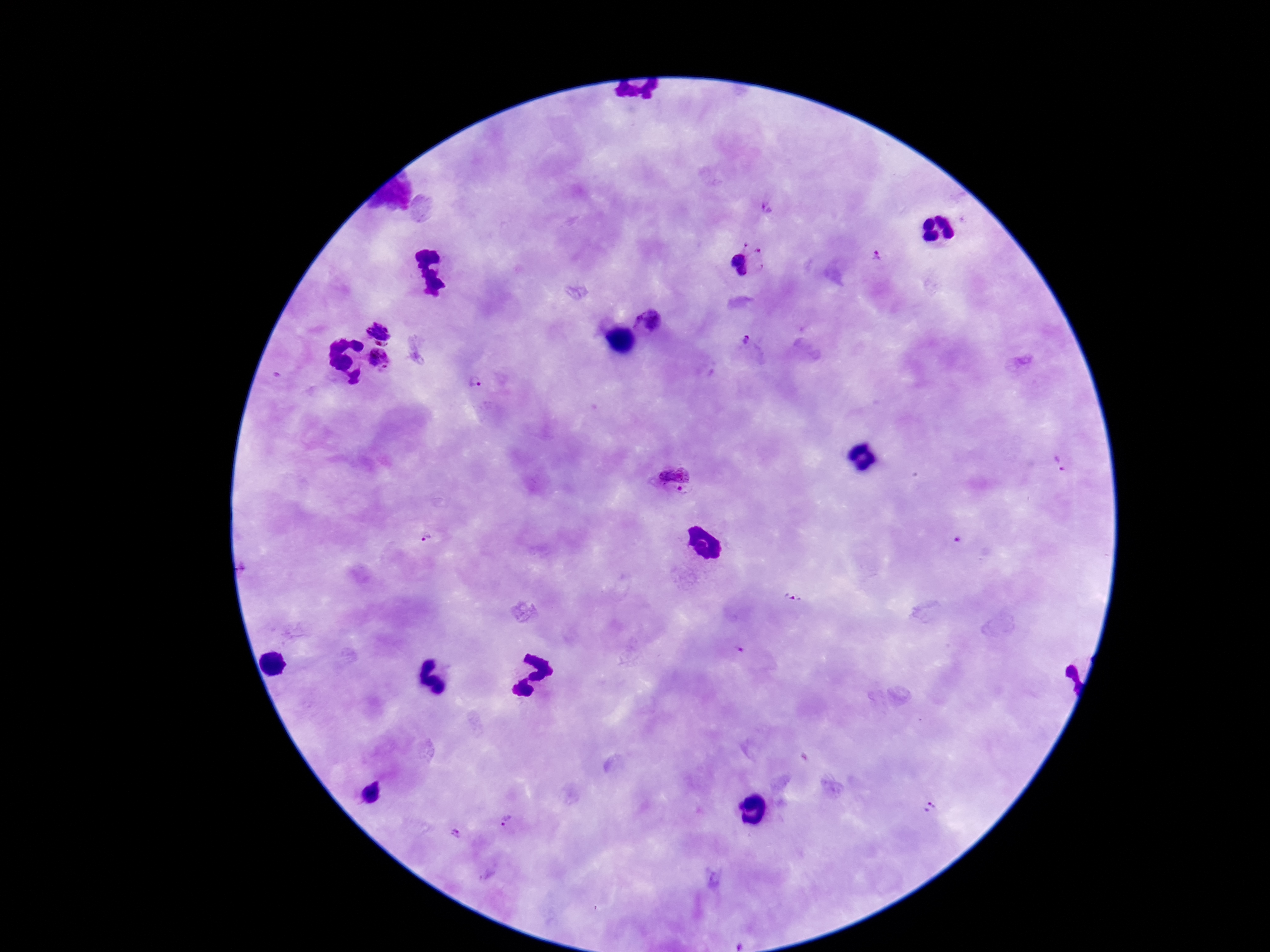
Approximate centers as {x, y} in pixels.
Summary:
  - Plasmodium parasite locations: {766, 209}, {876, 256}, {740, 264}, {652, 323}, {378, 331}, {748, 343}, {380, 360}, {476, 382}, {1058, 464}, {673, 478}, {426, 540}, {792, 597}, {740, 652}, {929, 810}, {508, 822}, {456, 833}
  - Image size: 1270×952 pixels
  - Magnification: 100x
  - Stain: Giemsa
  - Field of view: single
  - Capture: smartphone camera through the microscope eyepiece
  - Preparation: thick blood smear
  - Patient malaria status: positive